Name the parasite shown.
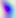

Toxoplasma gondii.

Summary:
  - Magnification: 400x
  - Modality: micrograph